Describe the morphology of the erythrocytes.
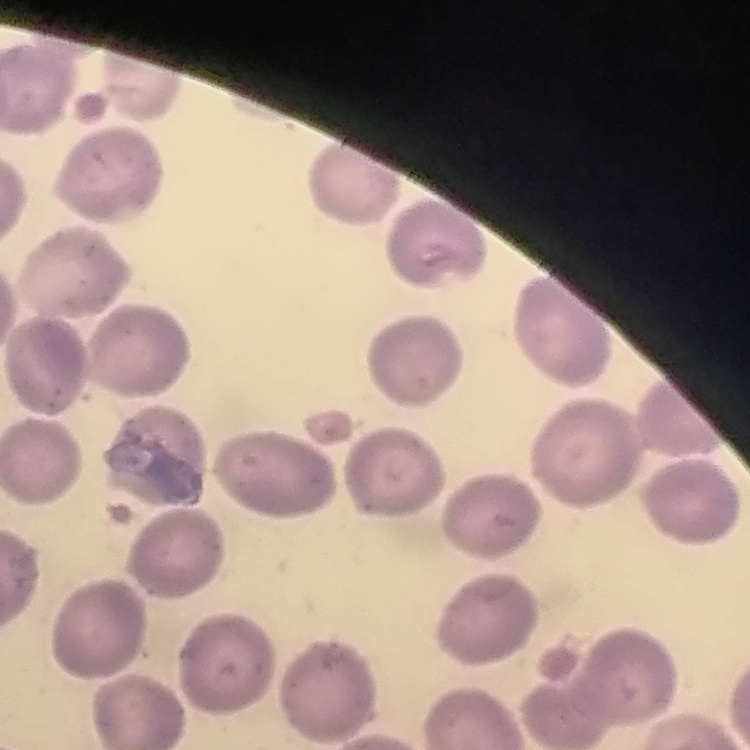

They show no rouleaux formation.

Summary:
  - Preparation: thin blood smear
  - Stain: Field's or Giemsa
  - Image type: one tile cut from a larger photomicrograph